Describe the morphology of the red blood cells.
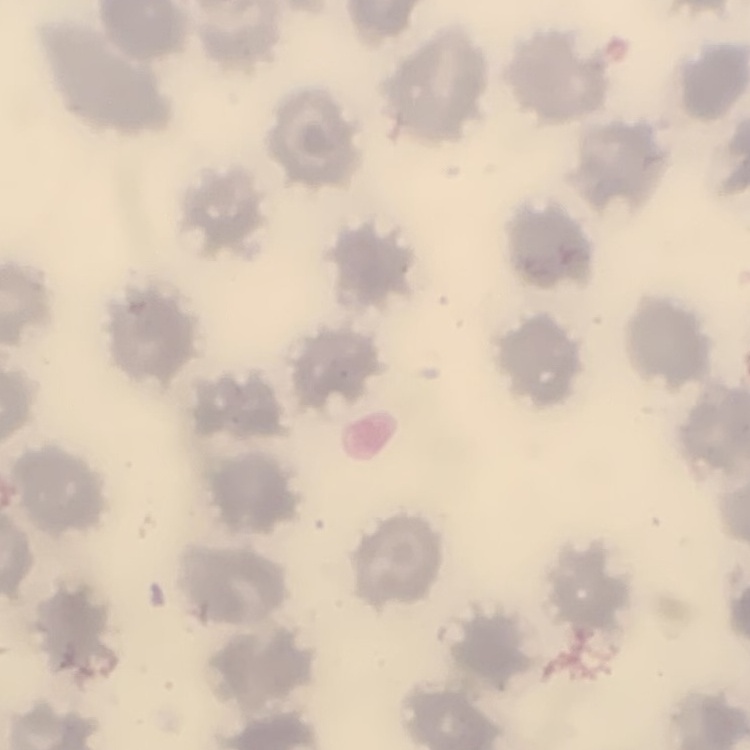

They show no rouleaux formation.

stain: Field's or Giemsa
image_type: one tile cut from a larger photomicrograph
preparation: thin peripheral smear